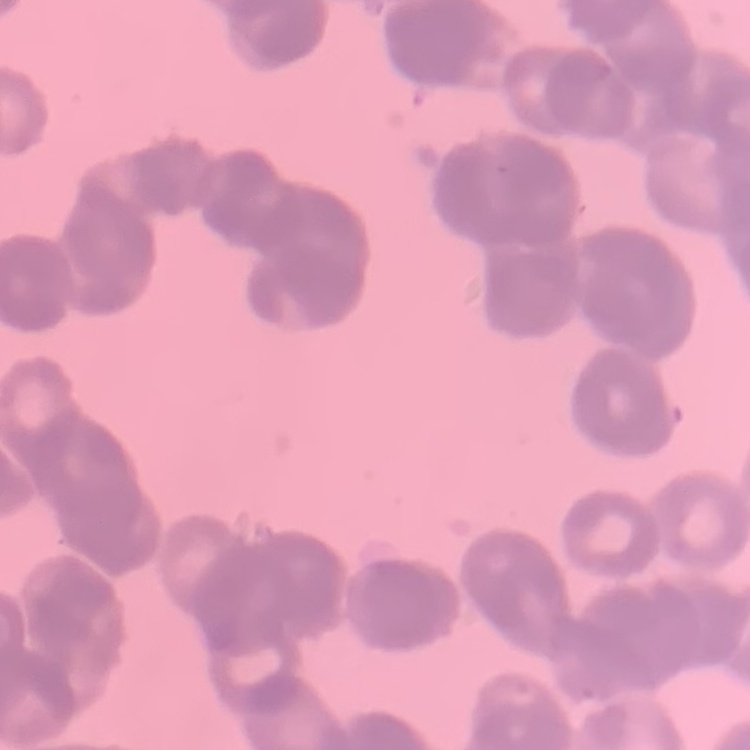
red blood cell morphology = rouleaux formation
preparation = thin blood smear
image type = square crop of a larger photomicrograph
stain = Field's or Giemsa